Give a bounding box for every parasitised red blood cell, every trophozoite, every gametocyte, every leukocyte, and every artifact (platelet-like body, stain precipitate, or debris).
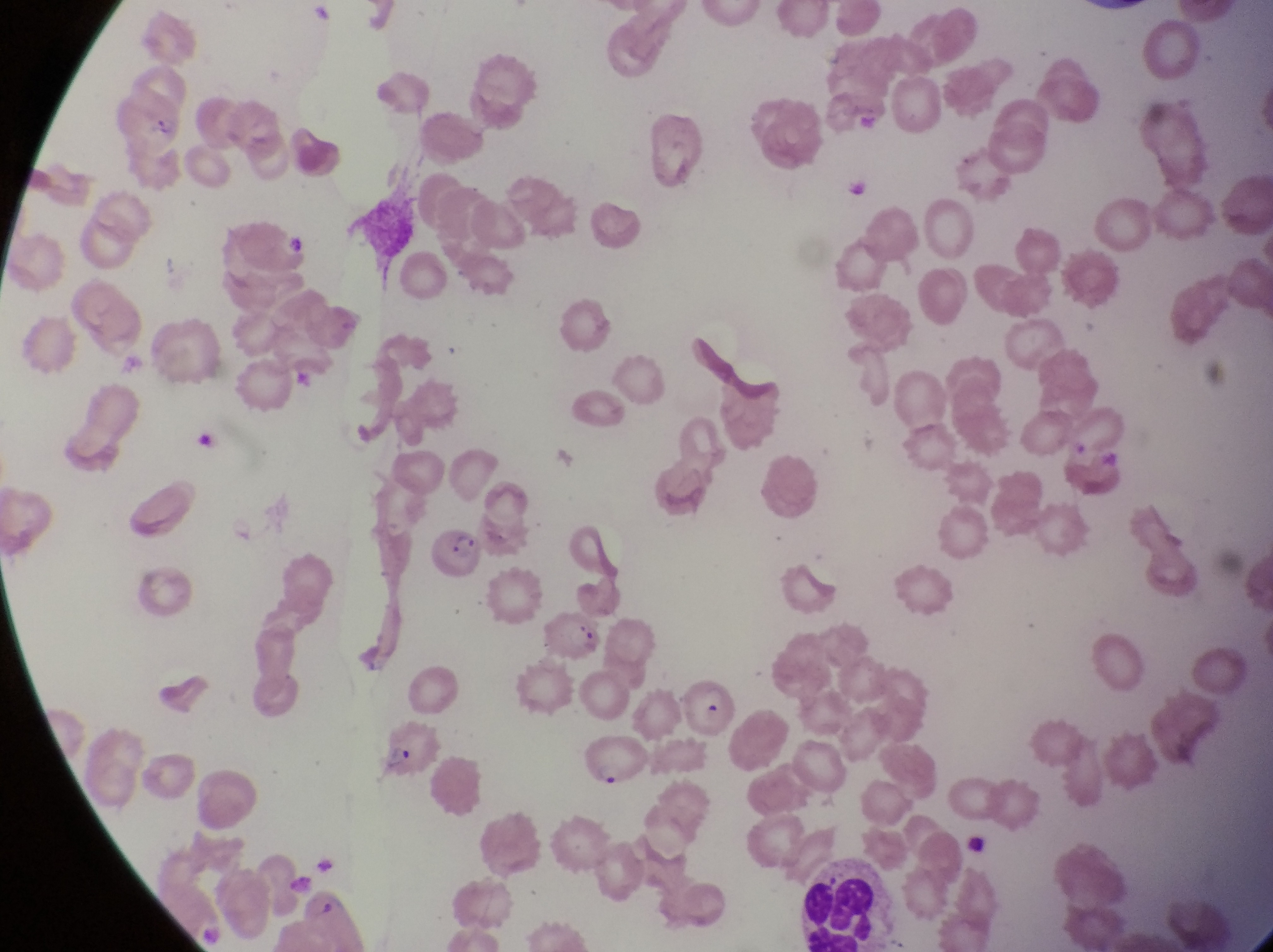

Approximate bounding boxes as (left, top, right, bottom) in pixels.
Parasitised red blood cells: (427, 522, 492, 579), (686, 669, 741, 734), (382, 726, 447, 779), (586, 729, 653, 786).
Leukocytes: (801, 854, 889, 951).

{
  "field_of_view": "single",
  "magnification": "1000x",
  "preparation": "thin blood film",
  "image_size": "1273×952 pixels",
  "country": "Uganda",
  "capture": "smartphone photograph through the eyepiece of an Olympus CX-23 microscope"
}